Assess this cell for malaria.
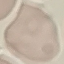
It is uninfected.

Summary:
  - Preparation: thin blood film
  - Capture: smartphone camera at the microscope eyepiece
  - Stain: Giemsa
  - Image type: automatically extracted cell patch, resized to 64 × 64 pixels